Assess the morphology of the erythrocytes.
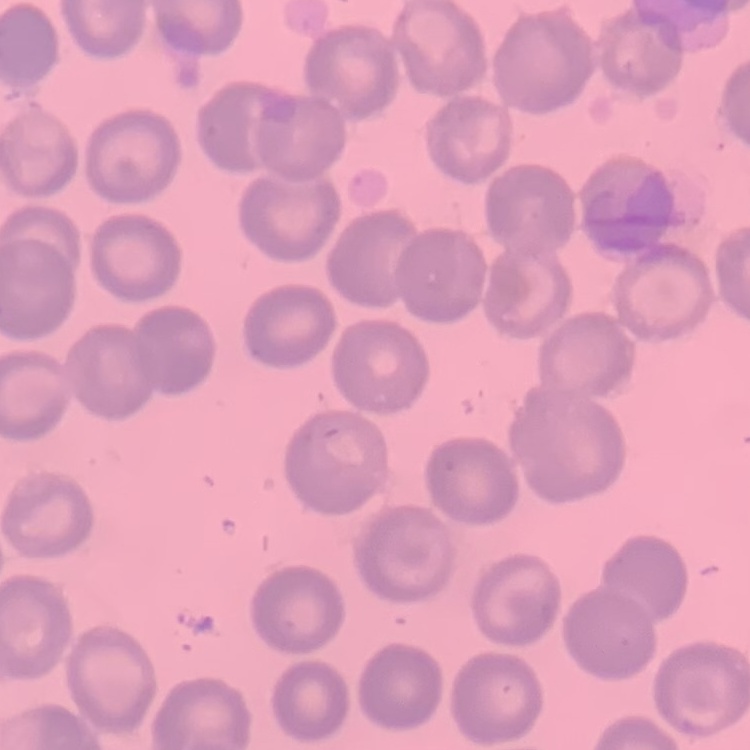

They show no rouleaux formation.

{
  "preparation": "thin peripheral smear",
  "image_type": "square crop of a larger photomicrograph",
  "stain": "Field's or Giemsa"
}